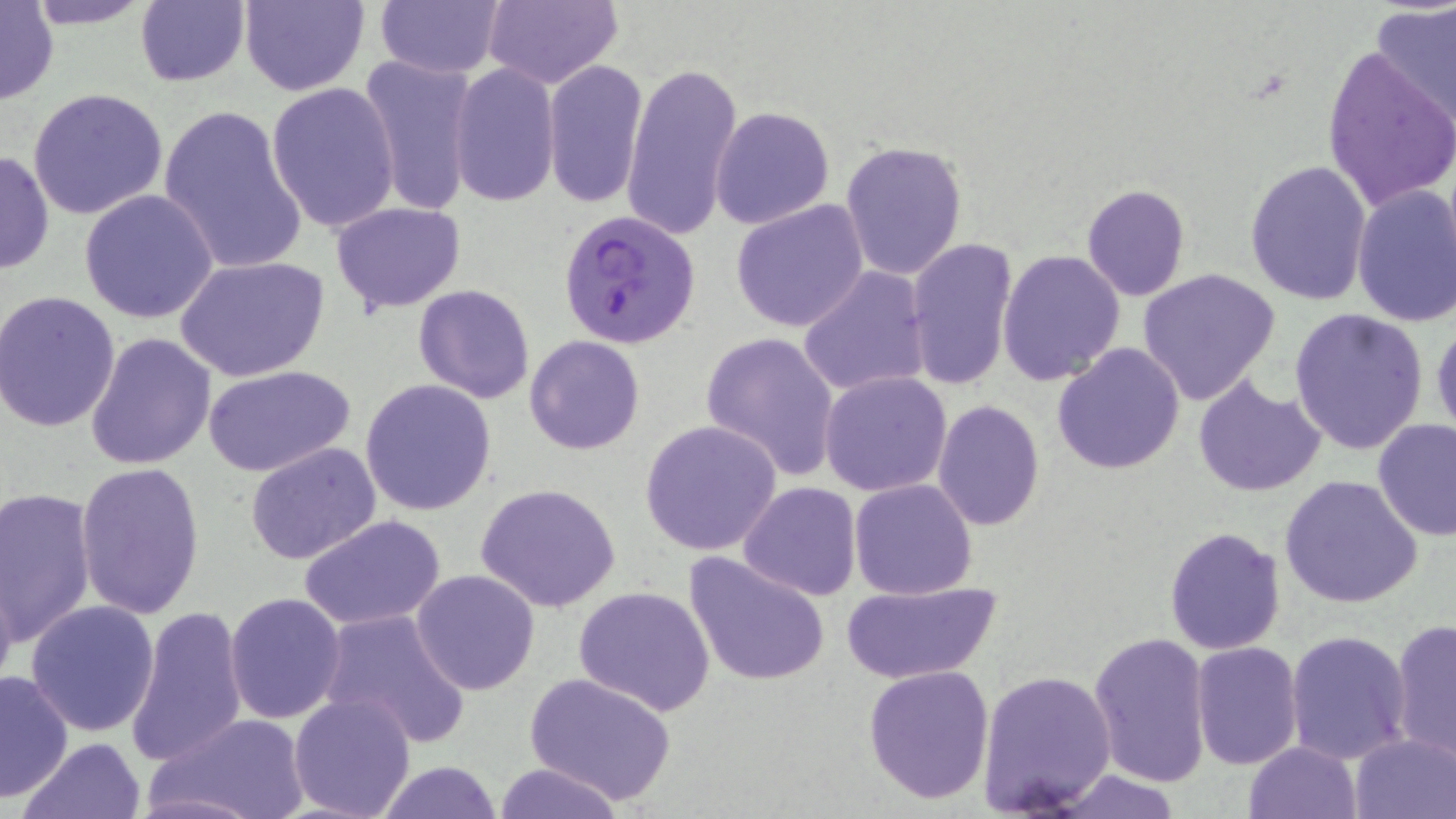

Approximate bounding boxes as (x1, y1, x2, y2) in pixels. Uninfected red blood cell locations: (21, 0, 160, 29), (239, 0, 368, 95), (372, 0, 508, 79), (483, 0, 625, 89), (134, 1, 250, 87), (0, 2, 58, 105), (1371, 2, 1456, 124), (1319, 40, 1456, 216), (358, 55, 479, 216), (542, 58, 648, 210), (625, 60, 744, 243), (447, 63, 560, 206), (265, 82, 401, 236), (27, 87, 169, 220), (158, 103, 307, 276), (710, 106, 835, 229), (840, 140, 967, 283), (0, 149, 54, 274), (1243, 160, 1373, 306), (1352, 183, 1456, 328), (1080, 185, 1190, 300), (78, 189, 221, 324), (330, 201, 467, 314), (730, 201, 869, 333), (905, 238, 1019, 391), (997, 249, 1126, 385), (174, 255, 329, 382), (1137, 266, 1282, 406), (799, 267, 932, 397), (413, 284, 537, 403), (0, 290, 122, 434), (1289, 307, 1429, 455), (1430, 316, 1456, 448), (85, 331, 216, 470), (701, 331, 842, 480), (524, 335, 645, 455), (1052, 343, 1186, 476), (203, 364, 356, 475), (820, 371, 952, 496), (1194, 375, 1325, 496), (360, 379, 496, 518), (933, 399, 1044, 533), (1373, 418, 1455, 540), (640, 420, 782, 557), (245, 442, 383, 564), (75, 463, 205, 619), (1279, 474, 1424, 610), (849, 478, 978, 600), (737, 482, 861, 601), (476, 483, 622, 613), (0, 486, 98, 649), (298, 514, 447, 628), (1163, 527, 1286, 655), (682, 550, 832, 688), (0, 566, 19, 707), (411, 570, 541, 696), (840, 578, 1001, 684), (573, 586, 714, 715), (225, 592, 346, 723), (26, 599, 161, 738), (123, 607, 249, 767), (316, 609, 472, 747), (1390, 619, 1455, 763), (1088, 630, 1213, 785), (1285, 630, 1413, 764), (1190, 642, 1304, 769), (863, 664, 995, 806), (977, 668, 1118, 815), (0, 670, 72, 799), (523, 670, 678, 806), (288, 691, 418, 819), (150, 712, 311, 819), (1349, 732, 1456, 817), (19, 736, 146, 819), (1245, 741, 1361, 818), (373, 761, 507, 818), (492, 761, 627, 818), (1045, 768, 1188, 819). Plasmodium falciparum-infected red blood cell locations: (558, 210, 701, 348). Slide-level diagnosis: Plasmodium falciparum. One field of a larger specimen. Optical microscopy. May-Grünwald-Giemsa stain. Thin blood smear. Image is 1456×819 pixels. 1000x magnification.